Name the blood parasite species.
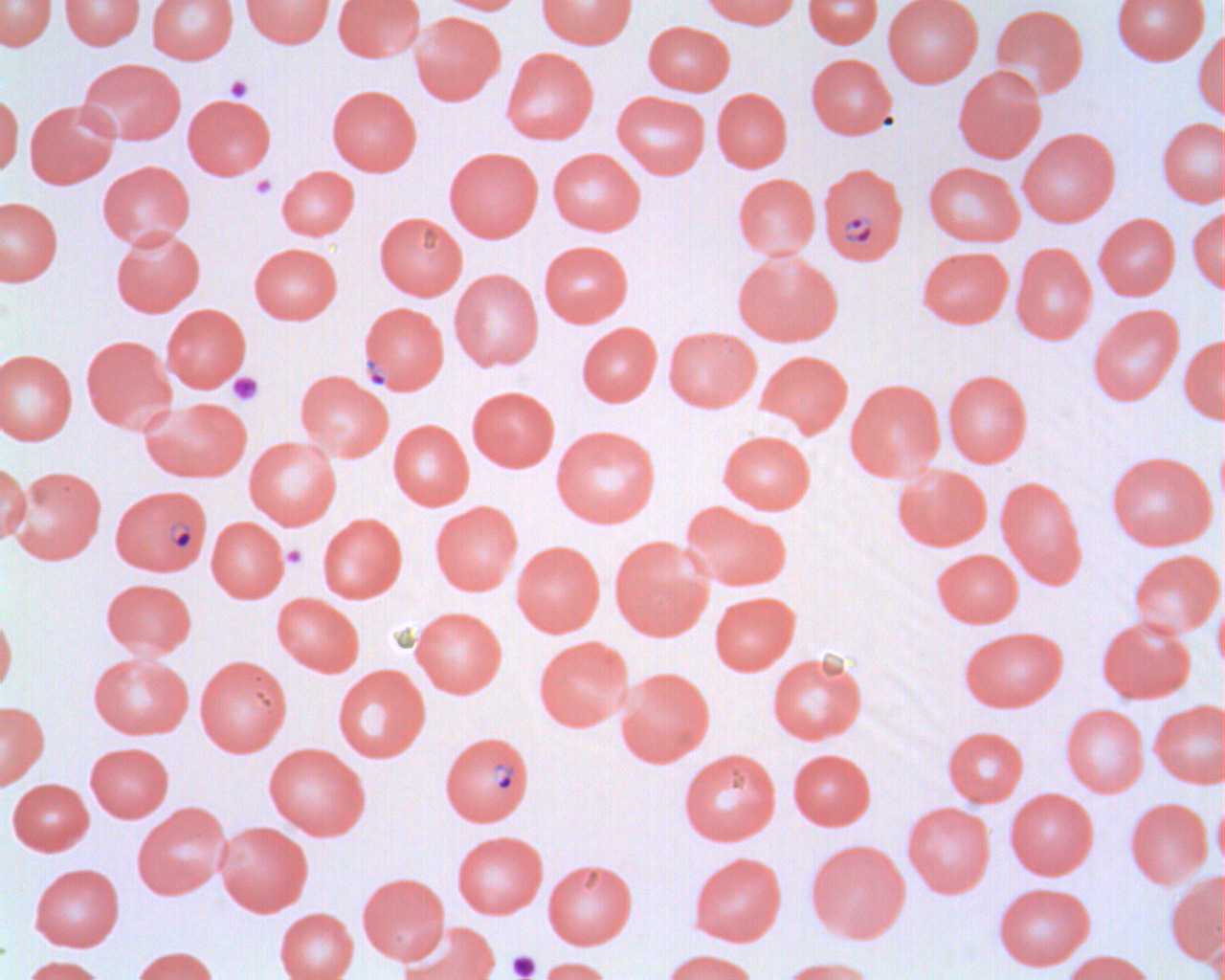

Plasmodium falciparum.

magnification = 1000x
platelet locations = approximate bounding boxes as named x1/y1/x2/y2 corners in pixels: (x1=225, y1=75, x2=253, y2=101), (x1=249, y1=175, x2=277, y2=199), (x1=228, y1=372, x2=263, y2=405), (x1=282, y1=544, x2=307, y2=568), (x1=507, y1=951, x2=541, y2=980)
modality = light microscopy
field of view = one of a larger specimen
preparation = thin blood smear
Plasmodium falciparum-infected red blood cell locations = approximate bounding boxes as named x1/y1/x2/y2 corners in pixels: (x1=818, y1=162, x2=909, y2=266), (x1=359, y1=301, x2=450, y2=395), (x1=111, y1=485, x2=212, y2=575), (x1=439, y1=731, x2=534, y2=826)
image size = 1225×980 pixels
uninfected red blood cell locations = approximate bounding boxes as named x1/y1/x2/y2 corners in pixels: (x1=0, y1=0, x2=57, y2=52), (x1=59, y1=0, x2=145, y2=50), (x1=147, y1=0, x2=238, y2=64), (x1=241, y1=0, x2=335, y2=47), (x1=333, y1=0, x2=425, y2=62), (x1=433, y1=0, x2=527, y2=14), (x1=536, y1=0, x2=637, y2=49), (x1=700, y1=0, x2=800, y2=29), (x1=804, y1=0, x2=883, y2=48), (x1=883, y1=0, x2=983, y2=87), (x1=1111, y1=0, x2=1209, y2=64), (x1=990, y1=3, x2=1088, y2=99), (x1=410, y1=11, x2=506, y2=105), (x1=643, y1=21, x2=735, y2=95), (x1=1193, y1=26, x2=1225, y2=122), (x1=501, y1=47, x2=599, y2=144), (x1=806, y1=53, x2=896, y2=139), (x1=78, y1=58, x2=185, y2=145), (x1=953, y1=66, x2=1046, y2=163), (x1=327, y1=85, x2=422, y2=175), (x1=712, y1=88, x2=792, y2=172), (x1=612, y1=90, x2=710, y2=178), (x1=0, y1=92, x2=24, y2=177), (x1=183, y1=94, x2=276, y2=179), (x1=24, y1=99, x2=120, y2=189), (x1=1156, y1=117, x2=1225, y2=207), (x1=1018, y1=128, x2=1120, y2=227), (x1=444, y1=147, x2=543, y2=242), (x1=547, y1=148, x2=646, y2=235), (x1=97, y1=161, x2=195, y2=248), (x1=923, y1=161, x2=1024, y2=246), (x1=277, y1=166, x2=359, y2=240), (x1=733, y1=173, x2=821, y2=260), (x1=0, y1=197, x2=63, y2=286), (x1=1187, y1=206, x2=1225, y2=294), (x1=375, y1=212, x2=467, y2=300), (x1=1093, y1=213, x2=1180, y2=299), (x1=110, y1=226, x2=205, y2=317), (x1=539, y1=240, x2=633, y2=327), (x1=249, y1=243, x2=343, y2=324), (x1=1011, y1=243, x2=1097, y2=345), (x1=918, y1=246, x2=1013, y2=328), (x1=733, y1=250, x2=842, y2=345), (x1=449, y1=269, x2=543, y2=371), (x1=162, y1=304, x2=251, y2=392), (x1=1087, y1=304, x2=1185, y2=406), (x1=577, y1=322, x2=662, y2=406), (x1=663, y1=327, x2=761, y2=412), (x1=1179, y1=334, x2=1225, y2=425), (x1=82, y1=335, x2=177, y2=433), (x1=0, y1=349, x2=77, y2=445), (x1=756, y1=350, x2=853, y2=438), (x1=943, y1=369, x2=1033, y2=467), (x1=296, y1=370, x2=394, y2=461), (x1=846, y1=378, x2=946, y2=481), (x1=467, y1=386, x2=559, y2=471), (x1=140, y1=397, x2=252, y2=482), (x1=388, y1=419, x2=474, y2=510), (x1=551, y1=425, x2=661, y2=528), (x1=718, y1=430, x2=816, y2=514), (x1=244, y1=436, x2=342, y2=529), (x1=1106, y1=450, x2=1216, y2=550), (x1=0, y1=461, x2=31, y2=545), (x1=892, y1=463, x2=992, y2=551), (x1=7, y1=465, x2=107, y2=565), (x1=996, y1=475, x2=1088, y2=588), (x1=431, y1=500, x2=523, y2=595), (x1=682, y1=502, x2=792, y2=591), (x1=317, y1=513, x2=407, y2=603), (x1=206, y1=516, x2=289, y2=602), (x1=610, y1=535, x2=713, y2=641), (x1=511, y1=540, x2=605, y2=636), (x1=932, y1=549, x2=1023, y2=627), (x1=1128, y1=549, x2=1225, y2=638), (x1=101, y1=578, x2=197, y2=657), (x1=709, y1=591, x2=800, y2=675), (x1=1213, y1=592, x2=1225, y2=677), (x1=272, y1=593, x2=364, y2=676), (x1=410, y1=606, x2=507, y2=697), (x1=0, y1=608, x2=17, y2=696), (x1=1097, y1=615, x2=1195, y2=703), (x1=960, y1=626, x2=1067, y2=712), (x1=534, y1=636, x2=634, y2=731), (x1=767, y1=651, x2=867, y2=744), (x1=88, y1=652, x2=193, y2=739), (x1=195, y1=655, x2=291, y2=756), (x1=333, y1=665, x2=430, y2=762), (x1=615, y1=667, x2=715, y2=767), (x1=1149, y1=699, x2=1225, y2=788), (x1=0, y1=701, x2=48, y2=790), (x1=1061, y1=704, x2=1149, y2=797), (x1=943, y1=726, x2=1028, y2=806), (x1=85, y1=742, x2=174, y2=822), (x1=264, y1=743, x2=370, y2=839), (x1=679, y1=748, x2=781, y2=845), (x1=788, y1=749, x2=875, y2=830), (x1=8, y1=779, x2=94, y2=855), (x1=1006, y1=788, x2=1098, y2=879), (x1=1213, y1=792, x2=1225, y2=878), (x1=1125, y1=797, x2=1212, y2=889), (x1=132, y1=802, x2=232, y2=899), (x1=902, y1=802, x2=996, y2=897), (x1=215, y1=821, x2=312, y2=916), (x1=452, y1=830, x2=547, y2=918), (x1=806, y1=839, x2=911, y2=943), (x1=689, y1=852, x2=786, y2=946), (x1=544, y1=859, x2=637, y2=949), (x1=29, y1=863, x2=124, y2=951), (x1=358, y1=872, x2=450, y2=964), (x1=1166, y1=872, x2=1225, y2=965), (x1=993, y1=882, x2=1095, y2=969), (x1=275, y1=908, x2=358, y2=980), (x1=1205, y1=910, x2=1225, y2=980), (x1=398, y1=921, x2=500, y2=980), (x1=131, y1=946, x2=219, y2=980), (x1=661, y1=949, x2=759, y2=980), (x1=1062, y1=949, x2=1156, y2=980), (x1=19, y1=955, x2=108, y2=980), (x1=534, y1=956, x2=615, y2=980), (x1=778, y1=956, x2=879, y2=980)